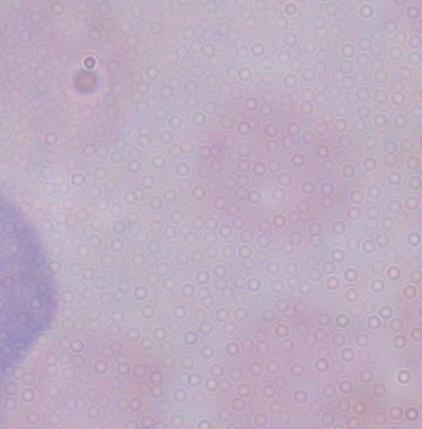
{
  "identification": "trypanosome",
  "modality": "micrograph",
  "magnification": "1000x"
}